Identify the parasite.
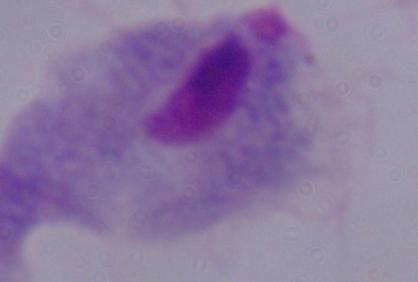

A trichomonad.

Micrograph. Captured at 1000x magnification.